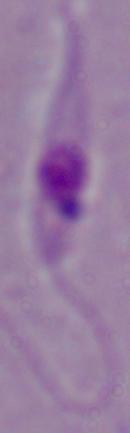 A Leishmania parasite is shown. Photomicrograph. 1000x magnification.